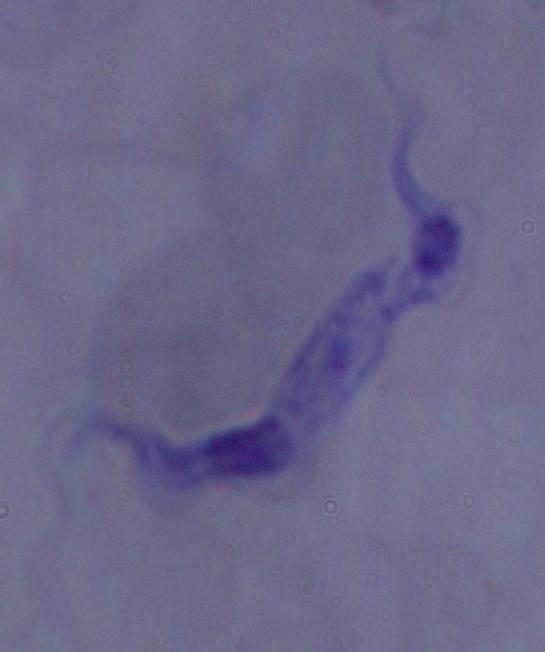
Summary:
  - Identification: trypanosome
  - Modality: photomicrograph
  - Magnification: 1000x